Report the malaria status of this cell.
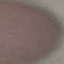

It is uninfected.

Thin blood film. Giemsa stain. Cell patch, automatically extracted from a larger field of view and resized to 64 × 64 pixels. Acquired by smartphone through the microscope eyepiece.